Report the malaria status of this cell.
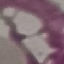

Uninfected.

capture = smartphone camera at the microscope eyepiece
preparation = thin blood film
stain = Giemsa
image type = cell patch, automatically extracted from a larger field of view and resized to 64 × 64 pixels